Comment on the morphology of the red blood cells.
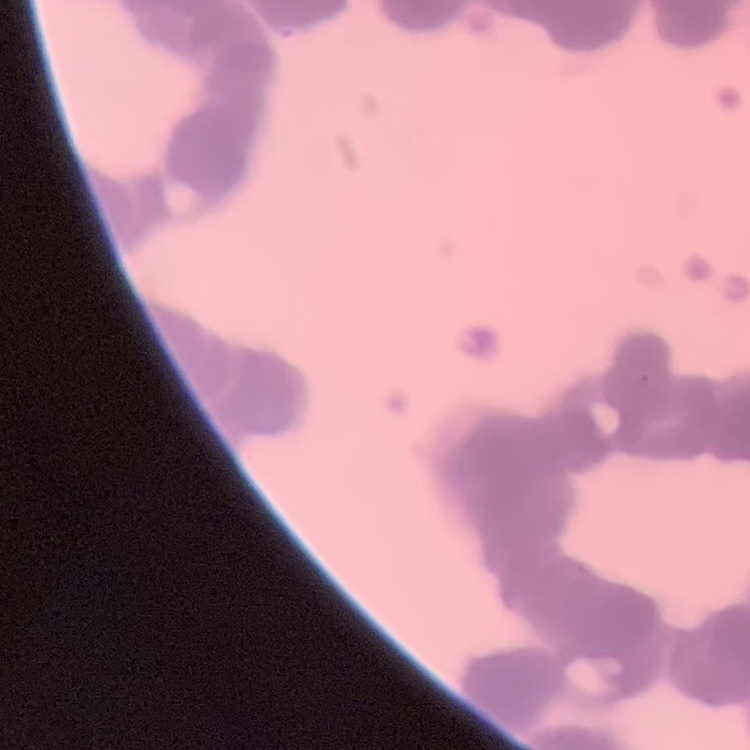

They show rouleaux formation.

Summary:
  - Preparation: thin blood smear
  - Image type: square crop of a larger photomicrograph
  - Stain: Field's or Giemsa